Locate every Plasmodium ovale-infected red blood cell.
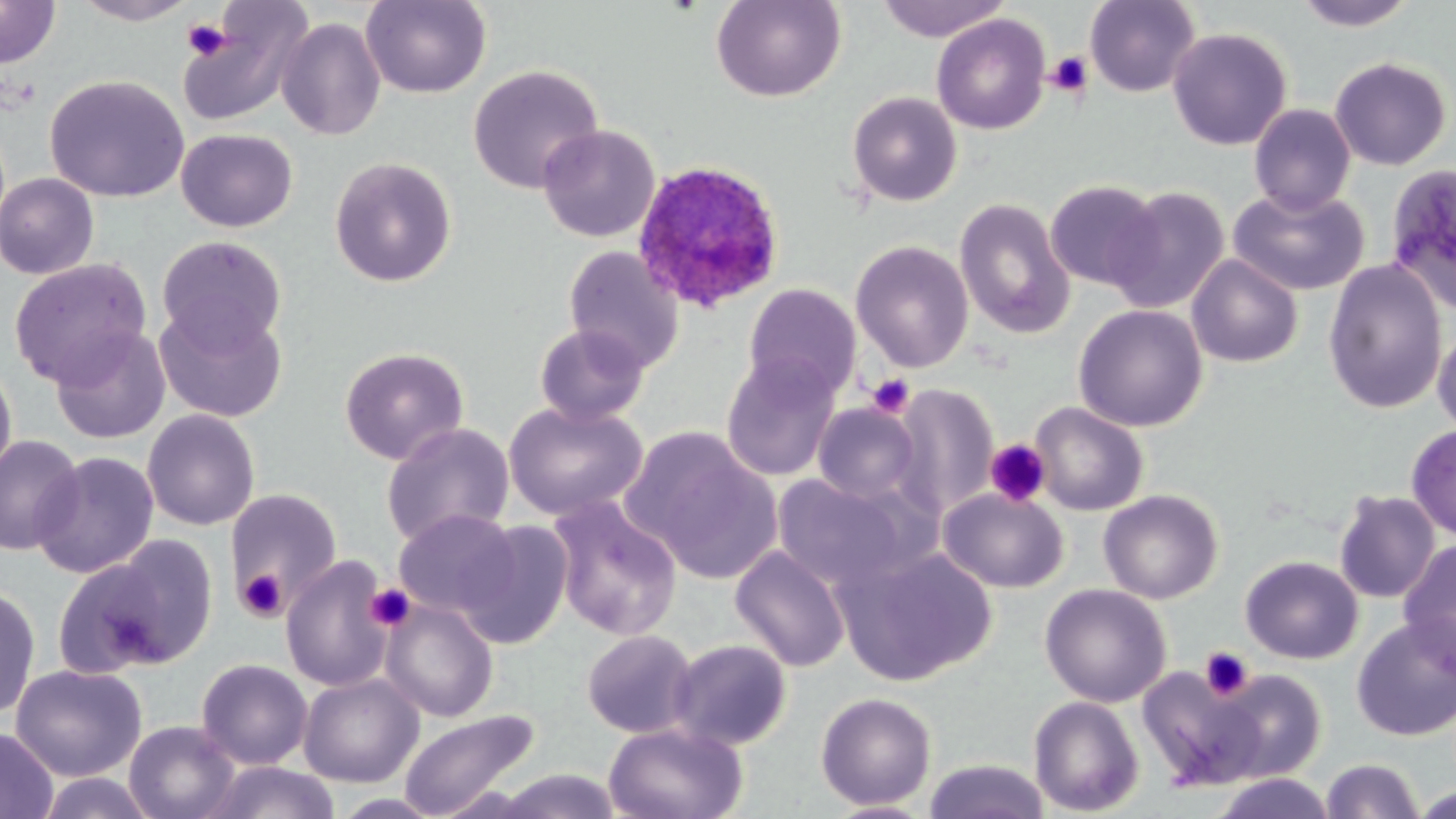

Approximate bounding boxes as [x1, y1, x2, y2] in pixels.
Plasmodium ovale-infected red blood cells: [629, 159, 788, 316].

slide-level diagnosis = Plasmodium ovale
stain = May-Grünwald-Giemsa
field of view = one of a larger specimen
uninfected red blood cell locations = approximate bounding boxes as [x1, y1, x2, y2] in pixels: [71, 0, 200, 25], [360, 0, 492, 98], [711, 0, 846, 103], [875, 0, 1011, 41], [1084, 0, 1200, 98], [1293, 0, 1417, 31], [0, 2, 61, 70], [180, 3, 314, 127], [931, 13, 1051, 135], [276, 17, 387, 141], [1167, 27, 1293, 151], [1329, 56, 1453, 170], [468, 64, 605, 194], [44, 74, 189, 203], [846, 91, 963, 207], [1249, 104, 1356, 215], [537, 124, 660, 243], [176, 128, 298, 232], [329, 156, 457, 287], [1385, 163, 1456, 313], [0, 172, 99, 280], [1044, 179, 1163, 290], [1106, 185, 1230, 313], [1229, 187, 1370, 296], [954, 198, 1075, 339], [156, 235, 287, 351], [850, 240, 974, 373], [563, 246, 685, 374], [1186, 254, 1304, 368], [9, 257, 152, 387], [1322, 260, 1448, 415], [743, 283, 862, 401], [153, 303, 288, 424], [1073, 304, 1208, 432], [1432, 321, 1456, 438], [534, 323, 650, 426], [49, 325, 171, 445], [45, 328, 167, 581], [339, 347, 469, 465], [721, 353, 842, 482], [0, 360, 17, 487], [890, 384, 998, 517], [503, 401, 648, 521], [813, 402, 922, 504], [1029, 402, 1148, 516], [142, 409, 261, 530], [380, 422, 515, 549], [1406, 424, 1456, 540], [626, 428, 783, 582], [1, 434, 84, 556], [31, 451, 158, 579], [773, 474, 915, 590], [938, 487, 1068, 593], [224, 489, 342, 611], [1098, 490, 1223, 604], [1334, 490, 1441, 604], [547, 495, 683, 641], [393, 509, 519, 619], [458, 520, 574, 649], [84, 536, 219, 673], [1397, 540, 1456, 678], [730, 546, 850, 672], [837, 546, 997, 686], [280, 555, 395, 693], [1240, 556, 1362, 664], [1231, 557, 1347, 777], [0, 583, 41, 721], [1039, 583, 1172, 707], [380, 598, 499, 722], [1351, 617, 1456, 742], [582, 629, 697, 739], [668, 639, 792, 750], [196, 658, 313, 770], [10, 663, 146, 781], [1136, 665, 1268, 791], [1212, 669, 1327, 783], [298, 673, 424, 788], [814, 692, 937, 811], [1028, 695, 1144, 816], [397, 709, 541, 819], [124, 720, 241, 819], [603, 721, 748, 819], [0, 727, 58, 819], [1320, 758, 1423, 818], [922, 759, 1051, 819], [198, 761, 343, 819], [493, 769, 624, 818], [1211, 772, 1336, 819], [1410, 785, 1455, 817], [822, 800, 937, 818]
platelet locations = approximate bounding boxes as [x1, y1, x2, y2] in pixels: [182, 19, 233, 60], [1045, 51, 1092, 98], [866, 373, 915, 419], [985, 439, 1052, 507], [237, 568, 288, 622], [365, 584, 416, 632], [1200, 646, 1255, 701]
image size = 1456×819 pixels
modality = light microscopy
preparation = thin blood smear
magnification = 1000x